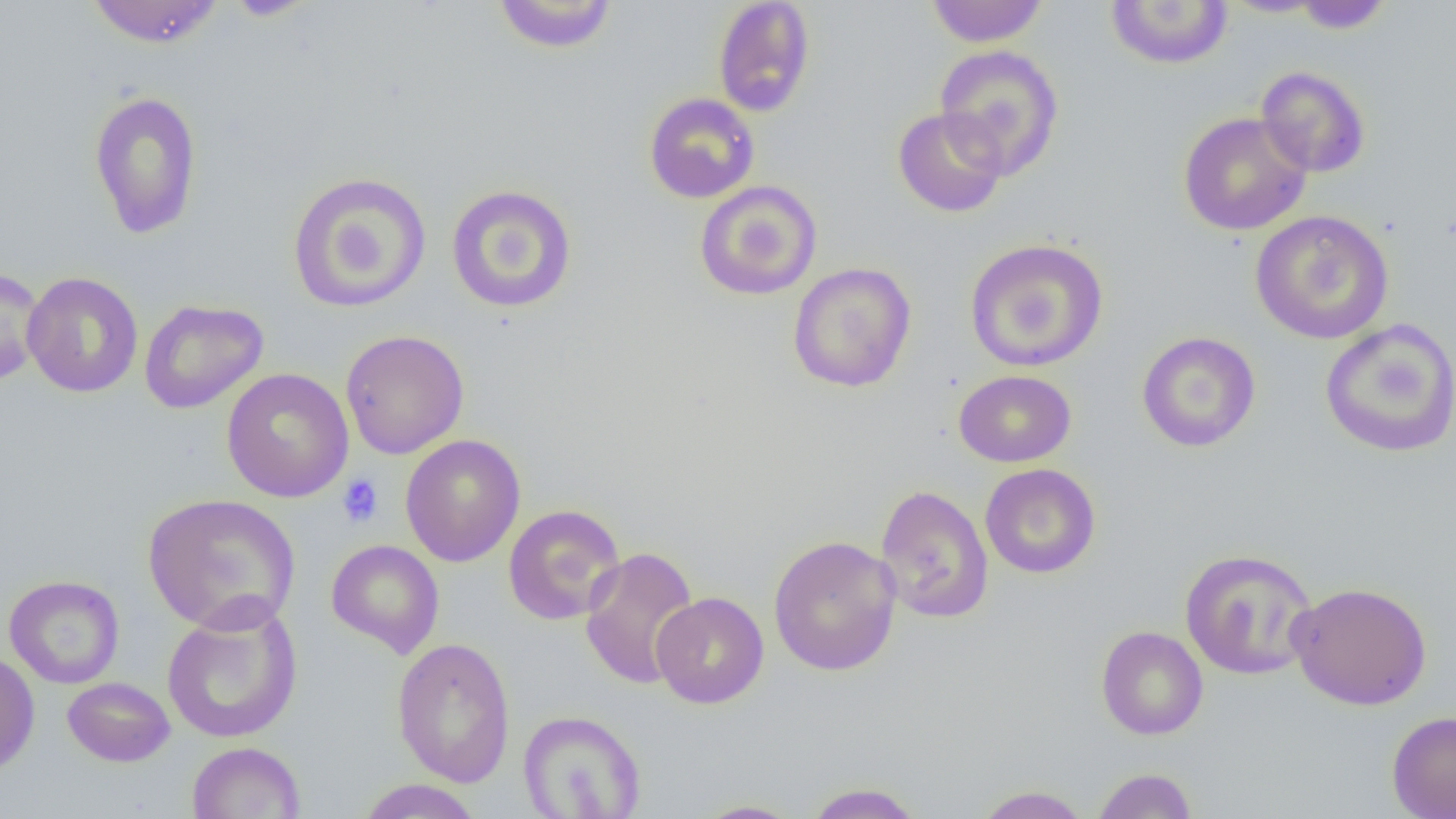

Approximate bounding boxes as (x1,y1)-(x2,y2) corner pairs in pixels. Platelet locations: (337,474)-(383,527). Uninfected red blood cell locations: (85,0)-(225,48), (222,0)-(319,20), (491,0)-(619,54), (713,0)-(816,117), (1291,0)-(1393,33), (924,1)-(1050,47), (1104,1)-(1233,70), (1219,1)-(1331,17), (933,44)-(1065,180), (1255,65)-(1371,178), (88,90)-(203,239), (644,92)-(760,204), (892,106)-(1008,218), (1178,111)-(1313,236), (287,171)-(432,313), (694,180)-(822,301), (446,183)-(577,313), (1249,210)-(1395,345), (964,237)-(1109,372), (787,262)-(917,393), (0,265)-(45,387), (22,271)-(143,398), (138,299)-(269,414), (1320,319)-(1456,458), (340,330)-(469,460), (1137,331)-(1261,453), (221,367)-(355,503), (953,370)-(1077,467), (400,434)-(525,567), (979,463)-(1101,579), (875,475)-(1102,593), (874,484)-(994,625), (143,493)-(301,634), (503,504)-(626,625), (768,535)-(902,676), (326,539)-(444,658), (579,546)-(700,690), (1179,548)-(1319,680), (4,574)-(124,688), (1287,581)-(1432,710), (650,591)-(768,708), (161,600)-(303,744), (1095,626)-(1208,740), (392,637)-(515,787), (0,650)-(39,775), (62,677)-(175,767), (518,709)-(647,819), (1386,710)-(1456,819), (187,741)-(305,819), (1091,767)-(1199,819), (356,778)-(483,818), (802,782)-(927,819), (971,784)-(1092,819), (690,799)-(806,818). Slide-level diagnosis: negative for blood parasites. Optical microscopy. 1000x magnification. Image is 1456×819 pixels. One field of a larger specimen. Thin blood film.